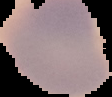

Summary:
  - Image size: 112×97 pixels
  - Result: no Plasmodium parasites detected
  - Image type: segmented cell region on a black background
  - Preparation: thin blood smear